Assess this cell for malaria.
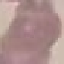
It is uninfected.

Automatically extracted cell patch, resized to 64 × 64 pixels. Acquired by smartphone through the microscope eyepiece. Thin blood film. Giemsa-stained preparation.